Identify the preparation type.
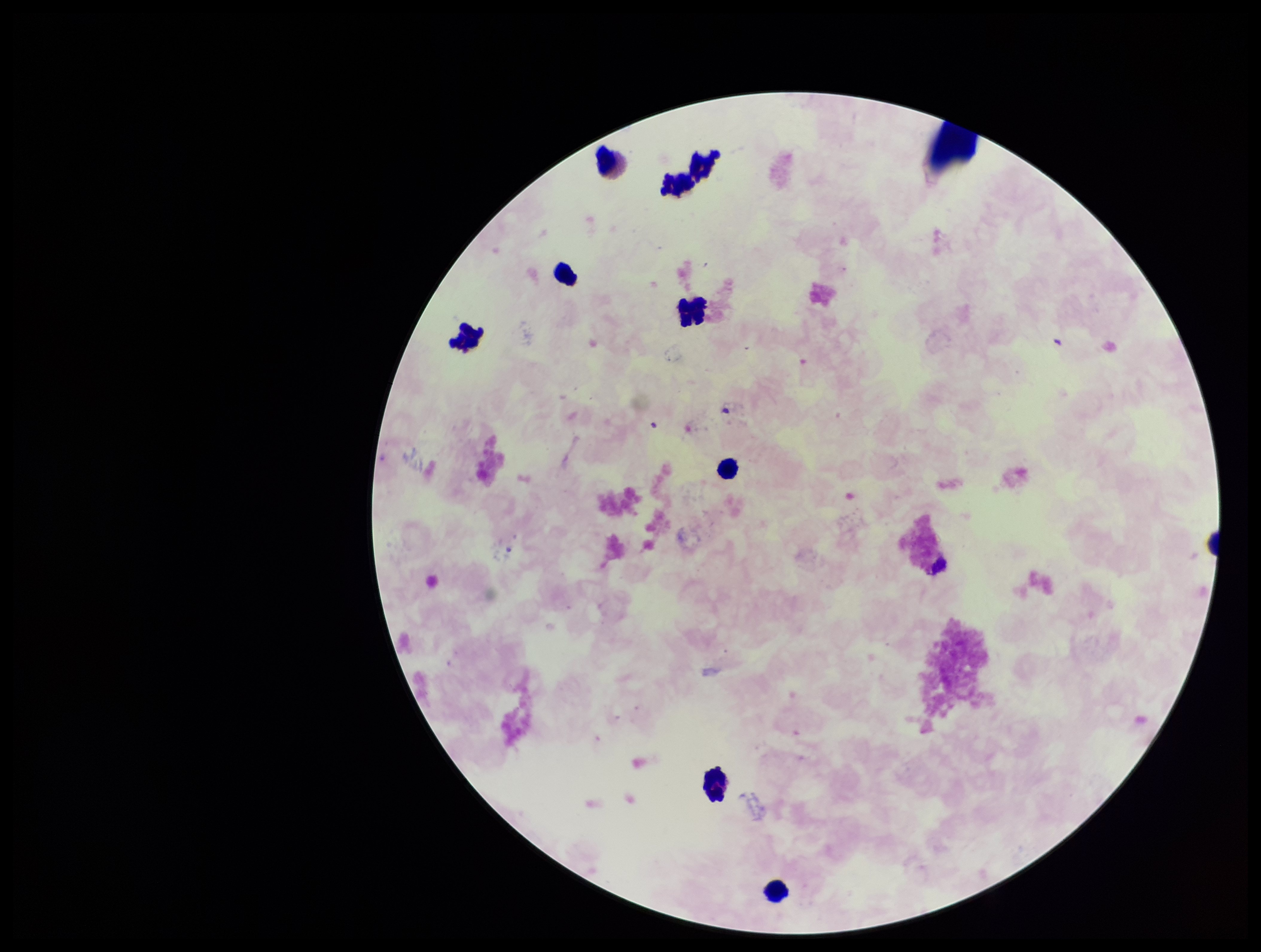
It is a thick blood smear.

Image is 1261×952 pixels. Smartphone photograph taken through the eyepiece of a microscope. Parasite count: 0. Single field of view. Stained with Giemsa. Plasmodium parasites: none identified. Leukocyte count: 9. Patient malaria status: negative.